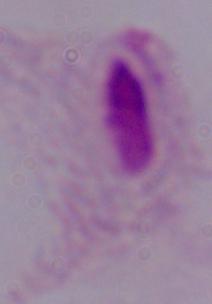

Micrograph. A trichomonad is seen. 1000x magnification.